Name the parasite shown.
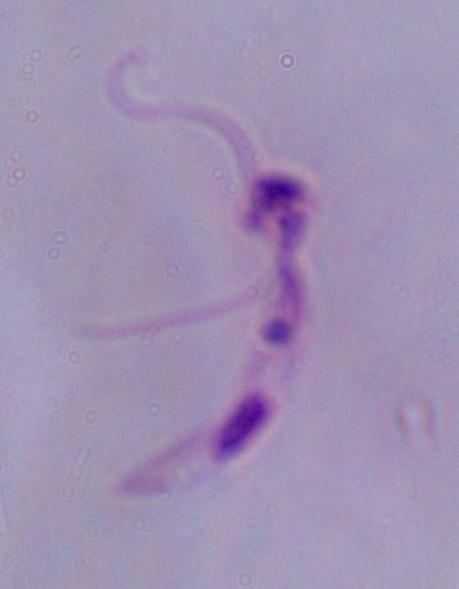
Leishmania.

Photomicrograph. Captured at 1000x magnification.